Describe the morphology of the red blood cells.
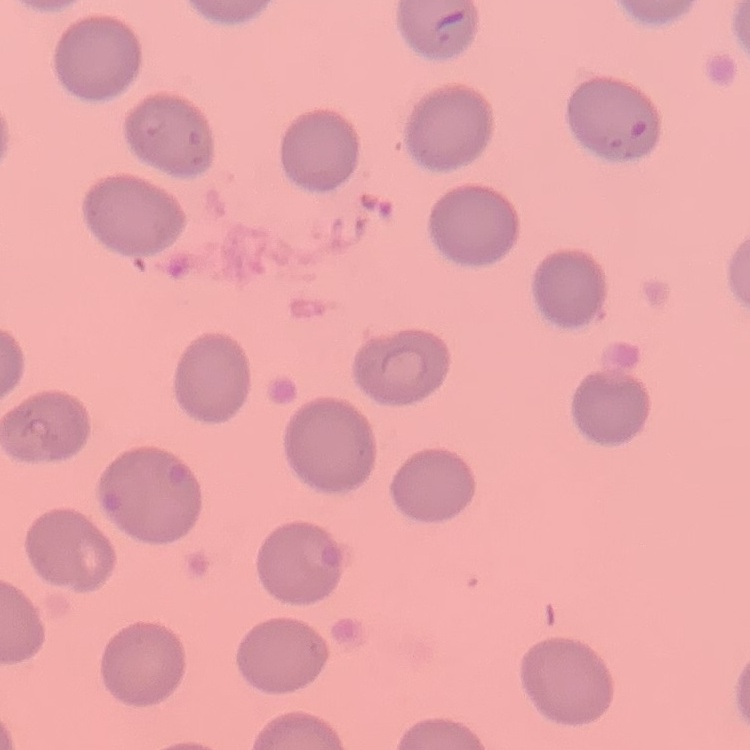

No rouleaux formation.

image type = square crop of a larger photomicrograph
preparation = thin blood smear
stain = Field's or Giemsa